Locate every Plasmodium parasite.
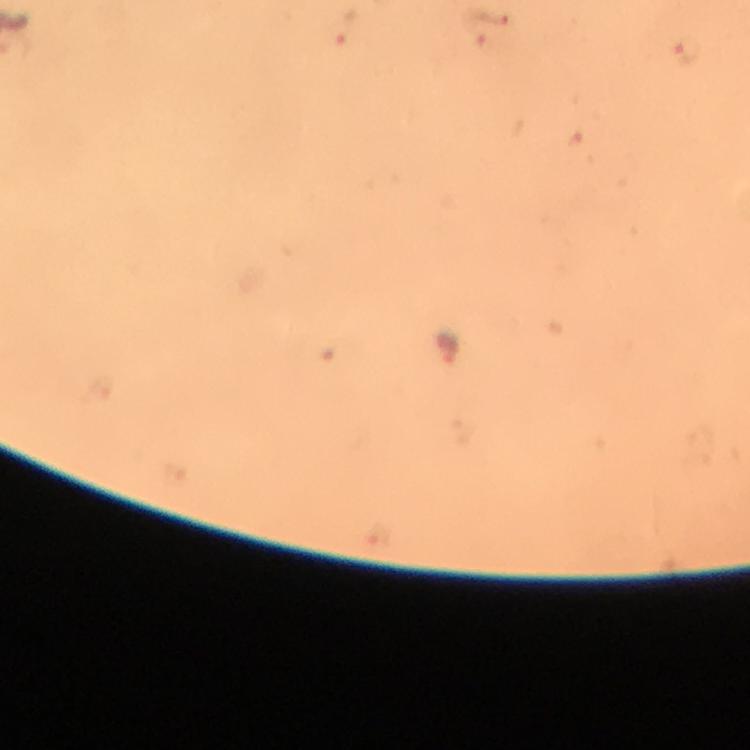
Approximate centers as (x, y) in pixels.
Plasmodium parasites: (487, 28), (339, 34), (685, 55), (447, 348).

Summary:
  - Stain: Giemsa
  - Preparation: thick smear
  - Cropped from: one field of view
  - Immersion oil: applied
  - Capture: smartphone camera through the microscope
  - Image size: 750×750 pixels
  - Context: from a malaria diagnostic workup
  - Magnification: 100x